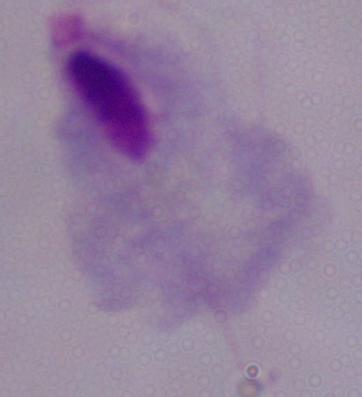
Summary:
  - Magnification: 1000x
  - Modality: photomicrograph
  - Identification: trichomonad